Identify the parasite.
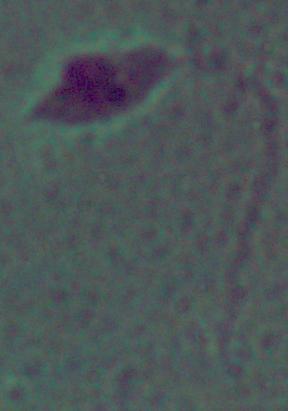

This is Leishmania.

{
  "magnification": "1000x",
  "modality": "micrograph"
}